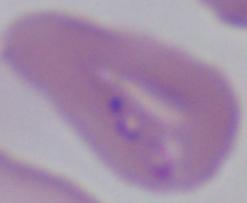
modality: photomicrograph
magnification: 1000x
identification: Babesia